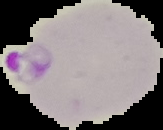

Summary:
  - Image size: 163×130 pixels
  - Result: Plasmodium parasites detected
  - Image type: cell region segmented out of the field of view; surrounding area masked to black
  - Preparation: thin blood smear